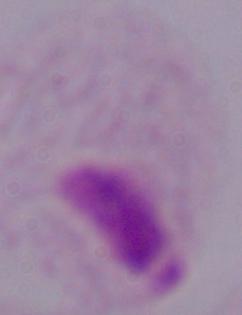
A trichomonad is shown. Micrograph. Captured at 1000x magnification.